Assess this cell for malaria.
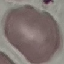

Uninfected.

Summary:
  - Preparation: thin blood smear
  - Image type: cell patch, automatically extracted from a larger field of view and resized to 64 × 64 pixels
  - Stain: Giemsa
  - Capture: smartphone through the microscope eyepiece